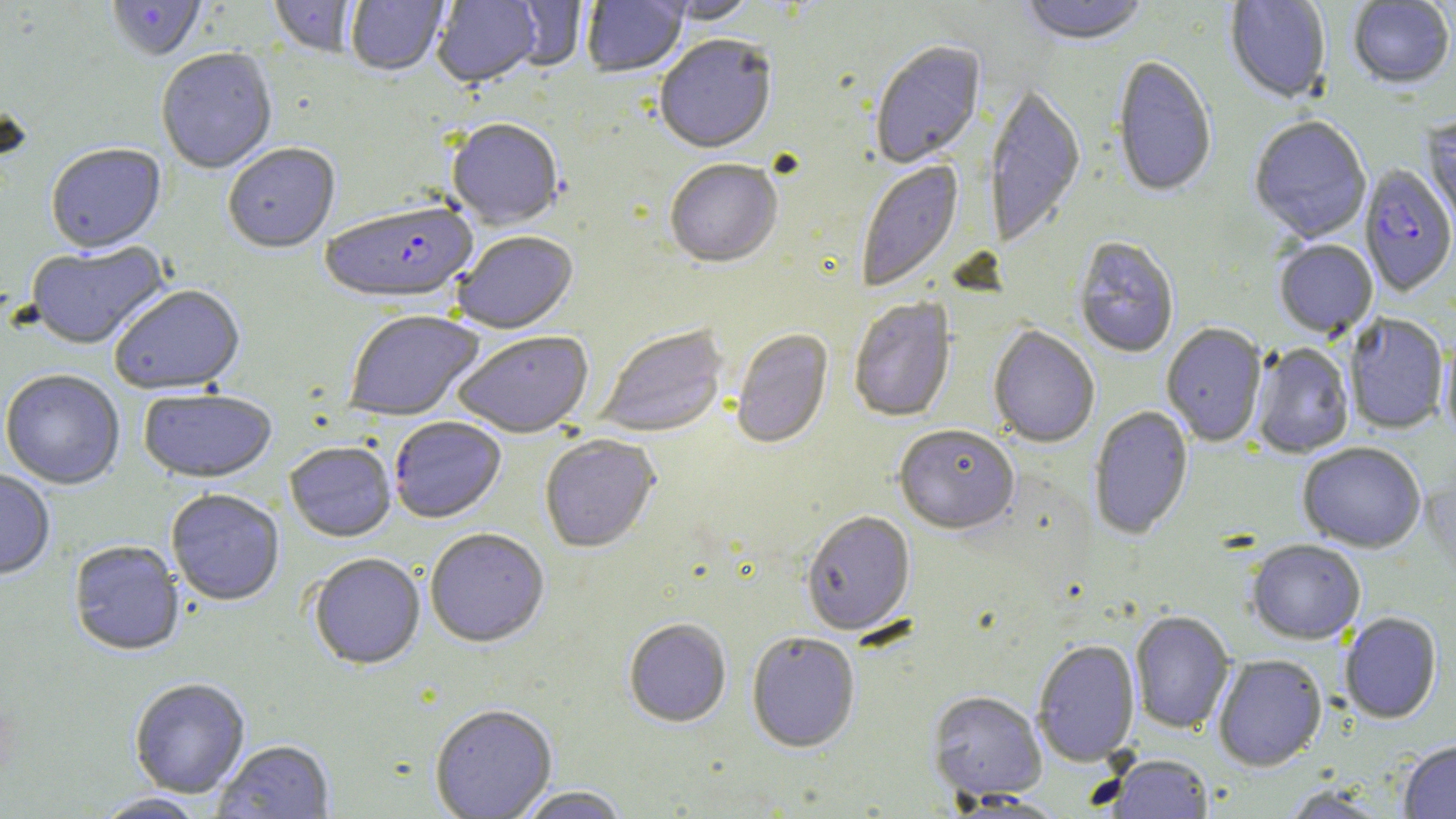 Approximate bounding boxes as (x1, y1, x2, y2) in pixels. Uninfected red blood cell locations: (107, 0, 206, 62), (269, 0, 362, 59), (431, 0, 541, 90), (582, 0, 688, 79), (1018, 0, 1149, 48), (1225, 0, 1331, 105), (346, 1, 448, 77), (504, 1, 588, 72), (653, 1, 760, 26), (1348, 1, 1455, 89), (655, 37, 777, 157), (870, 41, 986, 170), (156, 51, 278, 176), (1111, 58, 1217, 199), (984, 85, 1085, 250), (1421, 115, 1456, 237), (1249, 117, 1372, 243), (446, 121, 563, 233), (45, 145, 166, 256), (223, 145, 340, 256), (665, 161, 783, 270), (856, 161, 964, 293), (454, 234, 578, 336), (1073, 238, 1179, 359), (1274, 240, 1378, 339), (25, 241, 171, 351), (109, 286, 247, 396), (849, 298, 956, 423), (344, 312, 485, 422), (1344, 314, 1449, 435), (1161, 324, 1267, 448), (988, 326, 1100, 449), (596, 327, 728, 439), (731, 329, 834, 450), (453, 332, 594, 439), (1440, 336, 1456, 446), (1251, 343, 1354, 459), (0, 370, 125, 490), (138, 390, 277, 485), (1089, 406, 1193, 540), (390, 418, 506, 525), (893, 426, 1020, 536), (539, 436, 661, 554), (284, 443, 396, 543), (1297, 444, 1426, 554), (0, 470, 55, 581), (166, 490, 285, 607), (801, 512, 915, 637), (425, 529, 550, 649), (68, 541, 185, 657), (1247, 541, 1365, 645), (309, 554, 425, 671), (1129, 611, 1234, 734), (1339, 613, 1442, 724), (623, 619, 731, 728), (746, 632, 860, 753), (1032, 640, 1140, 765), (1213, 655, 1327, 771), (129, 679, 250, 799), (927, 691, 1047, 802), (430, 706, 557, 819), (1398, 740, 1456, 818), (214, 741, 336, 818), (1107, 754, 1213, 818), (1280, 785, 1395, 818), (516, 787, 630, 818), (93, 793, 208, 819). Plasmodium falciparum-infected red blood cell locations: (1359, 165, 1456, 298), (320, 206, 478, 308). Slide-level diagnosis: Plasmodium falciparum. Thin blood film. One field of a larger specimen. Image is 1456×819 pixels. 1000x magnification. Light microscopy. May-Grünwald-Giemsa-stained preparation.